Name the cell type shown.
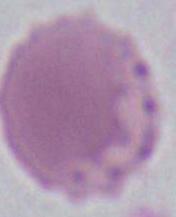
This is an erythrocyte.

Summary:
  - Modality: photomicrograph
  - Magnification: 1000x